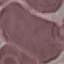

Result: no malaria parasites detected. Automatically extracted cell patch, resized to 64 × 64 pixels. Acquired by smartphone through the microscope eyepiece. Giemsa stain. Thin blood film.